Report the malaria status of this cell.
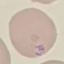

Parasitized.

Cell patch, automatically extracted from a larger field of view and resized to 64 × 64 pixels. Acquired by smartphone through the microscope eyepiece. Thin smear of blood. Giemsa stain.